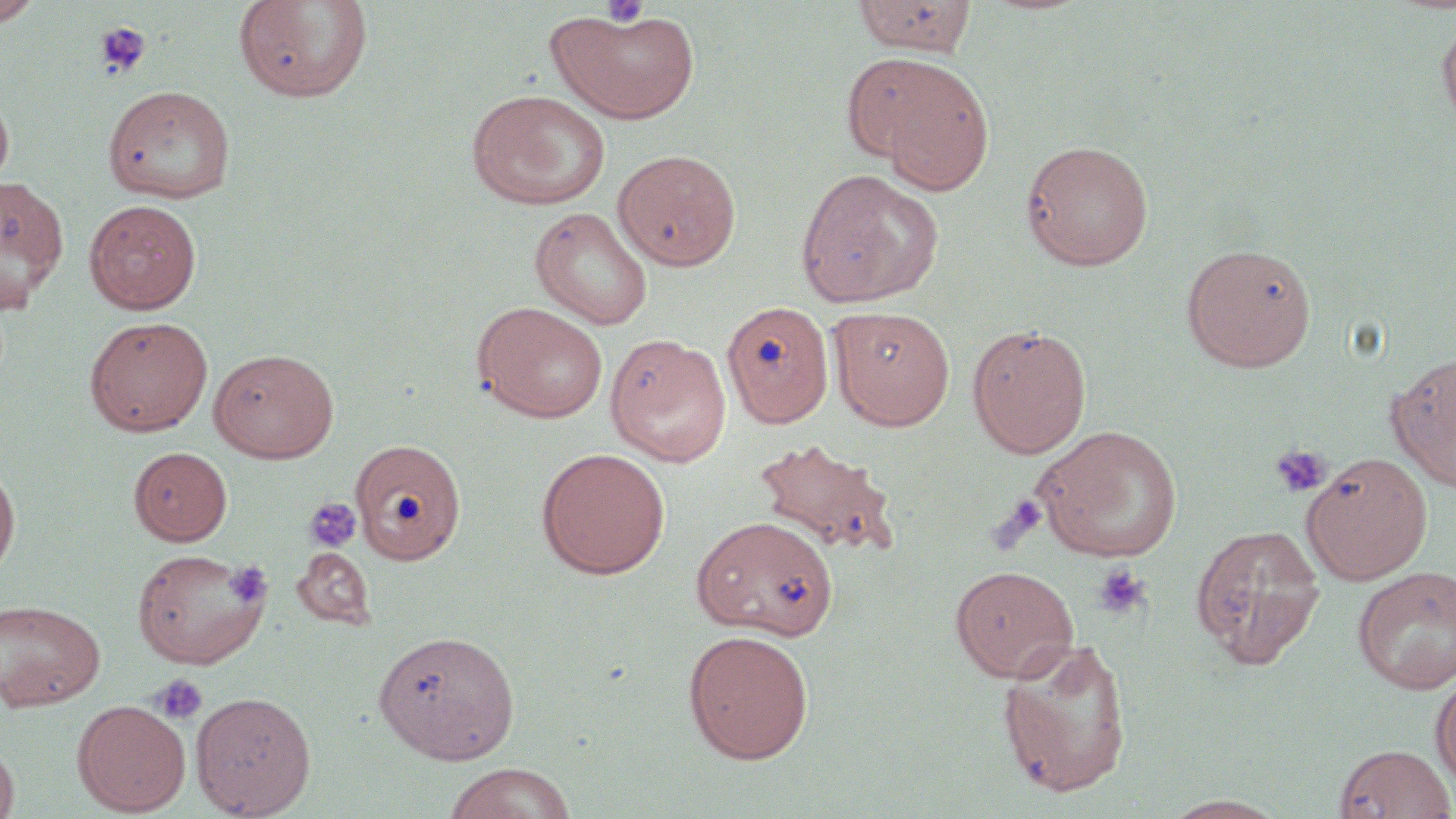
Summary:
  - Coordinate format: approximate bounding boxes as (x1,y1)-(x2,y2) corner pairs in pixels
  - Uninfected red blood cell locations: (0,0)-(43,25), (851,0)-(978,58), (233,1)-(374,104), (546,9)-(700,124), (1437,13)-(1456,128), (841,51)-(971,163), (875,69)-(994,195), (102,85)-(236,203), (0,87)-(14,189), (466,89)-(612,210), (1020,139)-(1154,271), (613,149)-(741,270), (795,168)-(944,307), (0,174)-(68,311), (83,199)-(202,314), (529,206)-(654,330), (1181,242)-(1317,371), (472,301)-(609,423), (721,301)-(834,428), (828,305)-(956,430), (84,316)-(213,435), (966,322)-(1092,458), (605,334)-(731,467), (209,347)-(339,463), (1387,348)-(1456,492), (1033,425)-(1184,563), (751,437)-(903,560), (349,439)-(466,565), (129,446)-(232,545), (536,447)-(671,580), (1301,451)-(1433,583), (0,458)-(20,580), (690,514)-(840,640), (1190,523)-(1327,668), (293,546)-(377,630), (131,547)-(270,669), (949,565)-(1078,682), (1352,565)-(1456,694), (1,598)-(106,711), (371,627)-(521,764), (682,628)-(815,764), (996,636)-(1134,799), (1430,673)-(1456,792), (190,691)-(316,817), (72,699)-(191,816), (0,738)-(19,819), (1333,742)-(1455,818), (442,762)-(578,819), (1162,794)-(1288,818)
  - Platelet locations: (600,1)-(652,29), (92,20)-(152,81), (1270,444)-(1331,498), (988,494)-(1048,554), (304,497)-(363,553), (225,561)-(272,607), (1091,562)-(1151,620), (153,674)-(208,725)
  - Slide-level diagnosis: negative for blood parasites
  - Magnification: 1000x
  - Image size: 1456×819 pixels
  - Modality: optical microscopy
  - Preparation: thin blood film
  - Stain: May-Grünwald-Giemsa
  - Field of view: one of a larger specimen